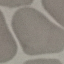

Summary:
  - Result: no malaria parasites detected
  - Preparation: thin blood smear
  - Stain: Giemsa
  - Image type: automatically extracted cell patch, resized to 64 × 64 pixels
  - Capture: smartphone through the microscope eyepiece